Classify this cell by malaria status.
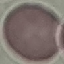

It is uninfected.

Automatically extracted cell patch, resized to 64 × 64 pixels. Acquired by smartphone through the microscope eyepiece. Thin blood smear. Giemsa-stained preparation.